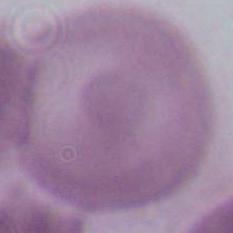
{
  "magnification": "1000x",
  "identification": "red blood cell",
  "modality": "micrograph"
}